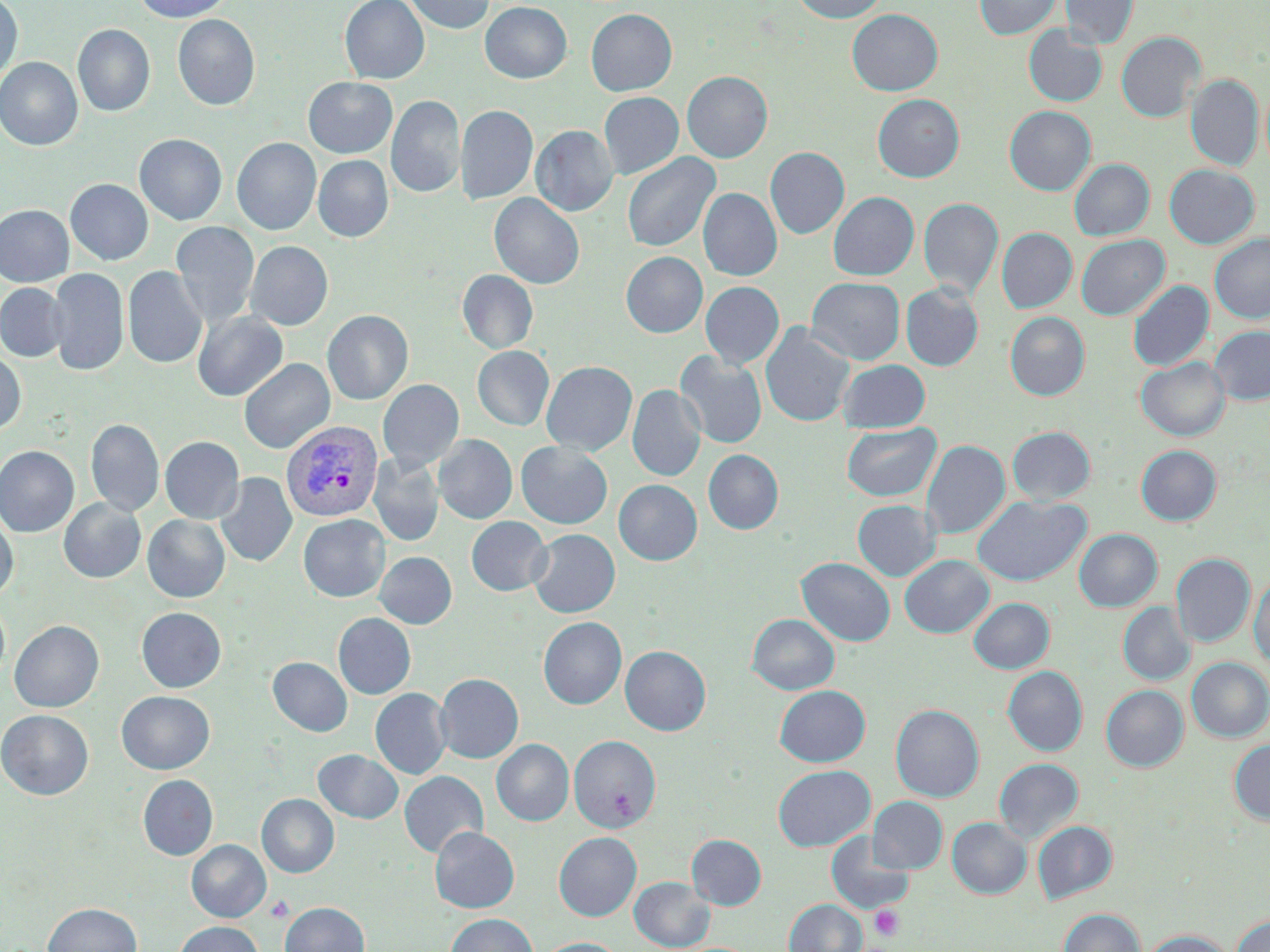
Summary:
  - Coordinate format: approximate bounding boxes as [x1, y1, x2, y2] in pixels
  - Uninfected red blood cell locations: [0, 0, 23, 84], [134, 0, 232, 22], [340, 0, 429, 84], [403, 0, 495, 34], [792, 0, 888, 23], [974, 0, 1062, 39], [1060, 0, 1139, 49], [480, 2, 572, 84], [586, 9, 677, 96], [846, 9, 943, 96], [173, 15, 260, 111], [73, 25, 155, 117], [1023, 25, 1108, 107], [1116, 32, 1205, 122], [0, 58, 83, 151], [682, 71, 772, 162], [1186, 74, 1263, 171], [303, 77, 397, 158], [599, 92, 684, 179], [872, 94, 964, 182], [386, 96, 465, 199], [455, 104, 538, 205], [1005, 106, 1095, 195], [531, 125, 618, 216], [134, 134, 227, 224], [232, 138, 321, 235], [765, 147, 849, 239], [622, 152, 720, 252], [313, 155, 393, 242], [1069, 159, 1154, 240], [1164, 164, 1259, 249], [65, 179, 153, 265], [698, 189, 782, 281], [828, 191, 919, 280], [489, 193, 584, 290], [919, 198, 1003, 298], [0, 205, 73, 287], [171, 221, 259, 328], [997, 228, 1077, 312], [1210, 232, 1270, 323], [1076, 235, 1169, 320], [245, 241, 333, 330], [621, 252, 707, 338], [123, 266, 208, 369], [48, 268, 129, 375], [457, 270, 538, 354], [806, 277, 905, 365], [1128, 280, 1213, 371], [700, 282, 784, 369], [0, 283, 68, 361], [901, 283, 984, 371], [192, 310, 288, 401], [323, 310, 413, 404], [1005, 312, 1090, 401], [760, 323, 854, 427], [1210, 326, 1270, 405], [472, 346, 554, 431], [0, 350, 26, 435], [675, 352, 767, 449], [1136, 357, 1230, 440], [239, 358, 335, 454], [838, 359, 930, 433], [541, 360, 637, 456], [378, 379, 464, 472], [627, 385, 705, 482], [86, 418, 164, 517], [841, 422, 941, 502], [1008, 426, 1095, 504], [434, 435, 517, 524], [160, 436, 244, 523], [922, 440, 1010, 540], [516, 442, 612, 529], [1136, 445, 1221, 525], [0, 446, 79, 537], [704, 449, 783, 534], [368, 454, 444, 546], [215, 472, 297, 567], [614, 479, 702, 565], [973, 495, 1090, 586], [59, 498, 146, 582], [852, 499, 941, 581], [0, 513, 18, 602], [298, 514, 390, 602], [142, 515, 230, 603], [466, 516, 551, 596], [528, 529, 620, 617], [1074, 529, 1162, 611], [375, 552, 457, 628], [1171, 553, 1255, 647], [899, 555, 994, 638], [797, 557, 895, 646], [1249, 572, 1270, 668], [969, 597, 1054, 673], [0, 600, 10, 685], [1118, 602, 1195, 685], [136, 607, 226, 692], [333, 613, 416, 699], [747, 614, 840, 695], [538, 617, 626, 709], [10, 620, 104, 712], [620, 645, 711, 735], [268, 657, 352, 736], [1186, 657, 1270, 742], [1003, 666, 1087, 756], [435, 673, 523, 763], [774, 685, 870, 767], [1101, 685, 1188, 771], [371, 688, 451, 779], [117, 691, 214, 774], [891, 704, 984, 801], [0, 710, 93, 799], [569, 735, 661, 832], [492, 739, 574, 826], [1229, 740, 1270, 825], [313, 749, 403, 823], [994, 758, 1083, 843], [773, 765, 874, 851], [399, 771, 488, 858], [138, 775, 218, 860], [257, 794, 339, 877], [868, 796, 948, 874], [947, 817, 1031, 898], [1032, 820, 1117, 903], [430, 826, 519, 913], [554, 832, 641, 921], [826, 832, 914, 914], [687, 834, 766, 909], [187, 840, 270, 922], [629, 877, 715, 951], [784, 899, 866, 952], [280, 901, 370, 952], [43, 902, 141, 952], [1059, 908, 1145, 952], [446, 913, 538, 952], [1231, 914, 1270, 952], [174, 921, 263, 952], [1141, 929, 1236, 952], [537, 937, 623, 952]
  - Plasmodium vivax-infected red blood cell locations: [281, 421, 383, 522]
  - Platelet locations: [265, 895, 294, 922], [870, 905, 904, 941]
  - Slide-level diagnosis: Plasmodium vivax
  - Preparation: thin blood film
  - Modality: light microscopy
  - Field of view: one of a larger specimen
  - Stain: May-Grünwald-Giemsa
  - Magnification: 1000x
  - Image size: 1270×952 pixels